Report the malaria status of this cell.
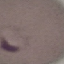
Parasitized.

Summary:
  - Stain: Giemsa
  - Image type: cell patch, automatically extracted from a larger field of view and resized to 64 × 64 pixels
  - Preparation: thin blood smear
  - Capture: smartphone camera at the microscope eyepiece